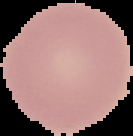
preparation = thin blood film
image type = segmented cell region with the area outside set to black
image size = 133×136 pixels
result = negative for malaria parasites